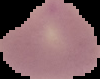
image size = 100×79 pixels
malaria status = parasitized
preparation = thin blood film
image type = segmented cell region on a black background